Outline each Plasmodium falciparum-infected red blood cell.
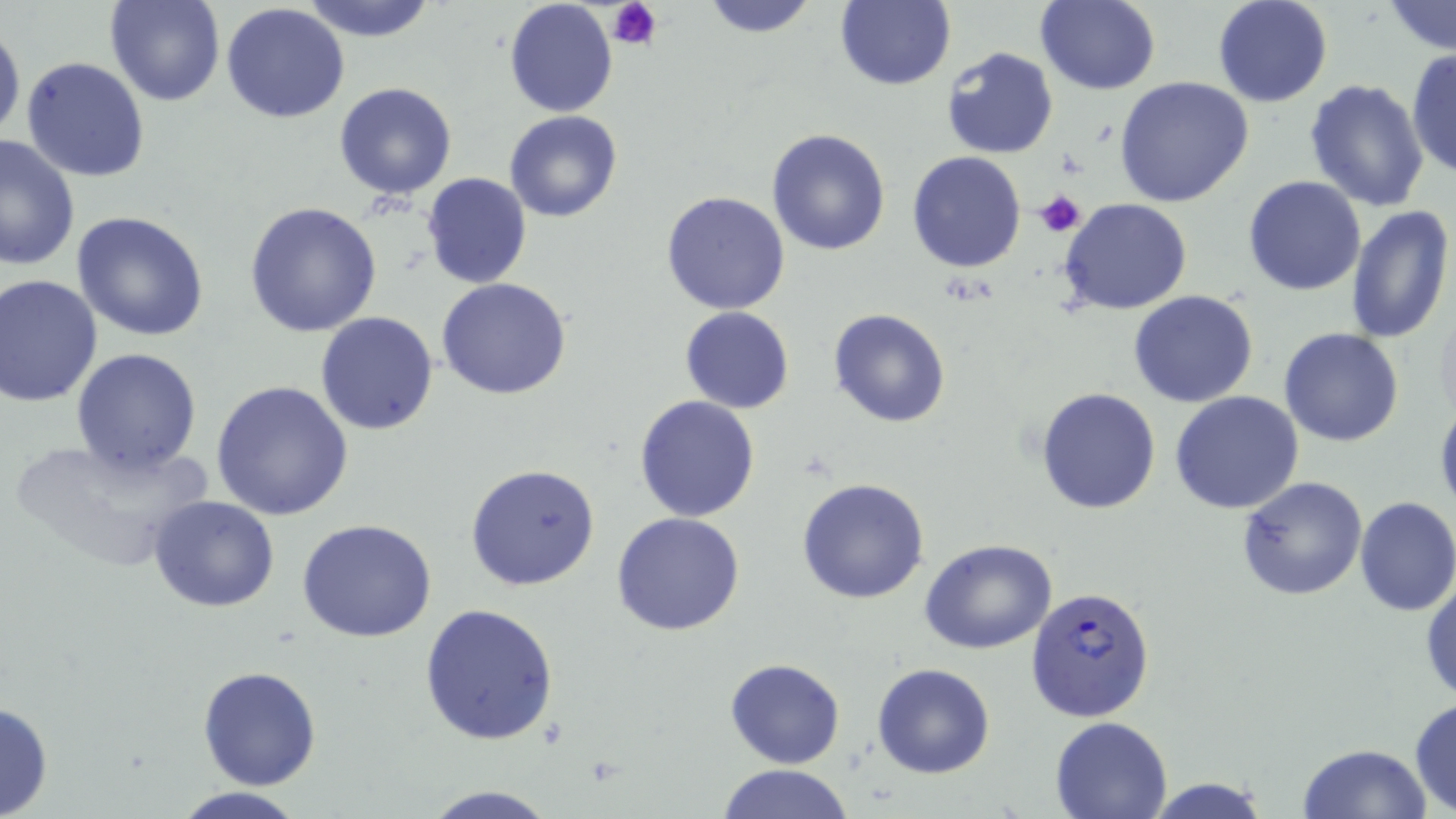
Approximate bounding boxes as (x1, y1, x2, y2) in pixels.
Plasmodium falciparum-infected red blood cells: (1025, 582, 1154, 724).

slide_level_diagnosis: Plasmodium falciparum
uninfected_red_blood_cell_locations: 'approximate bounding boxes as (x1, y1, x2, y2) in pixels: (105, 0, 226, 107), (299, 0, 438, 42), (502, 0, 619, 118), (697, 0, 825, 37), (832, 0, 956, 90), (1211, 0, 1333, 108), (1036, 1, 1162, 96), (1384, 2, 1455, 54), (221, 3, 350, 123), (0, 18, 24, 145), (943, 47, 1059, 160), (1406, 47, 1456, 181), (21, 55, 151, 184), (1113, 76, 1253, 208), (1305, 78, 1432, 213), (334, 83, 458, 200), (504, 110, 625, 223), (450, 124, 577, 251), (766, 128, 892, 256), (0, 132, 79, 271), (907, 151, 1029, 273), (421, 173, 532, 291), (1243, 176, 1366, 295), (661, 190, 791, 315), (1059, 199, 1192, 316), (244, 202, 382, 336), (1344, 203, 1454, 345), (70, 210, 210, 342), (0, 275, 102, 407), (436, 278, 572, 401), (1128, 290, 1259, 408), (680, 307, 794, 413), (828, 309, 952, 428), (315, 312, 439, 435), (1279, 328, 1404, 446), (71, 348, 202, 477), (210, 381, 354, 522), (1036, 388, 1161, 515), (1170, 391, 1305, 514), (634, 394, 761, 522), (1435, 400, 1456, 522), (10, 437, 210, 572), (466, 463, 600, 591), (1236, 477, 1369, 601), (796, 478, 930, 604), (148, 495, 279, 612), (1354, 497, 1456, 617), (612, 512, 746, 636), (298, 519, 439, 643), (919, 539, 1060, 655), (1421, 570, 1456, 704), (419, 602, 559, 745), (725, 658, 846, 768), (872, 663, 995, 779), (198, 665, 322, 790), (1408, 698, 1456, 816), (0, 700, 53, 819), (1050, 716, 1174, 818), (1299, 744, 1431, 819), (714, 764, 856, 819), (1142, 777, 1275, 818), (419, 784, 561, 819), (168, 787, 311, 819)'
field_of_view: one of a larger specimen
magnification: 1000x
modality: light microscopy
preparation: thin blood smear
stain: May-Grünwald-Giemsa
platelet_locations: 'approximate bounding boxes as (x1, y1, x2, y2) in pixels: (608, 0, 663, 49), (1034, 189, 1085, 236)'
image_size: 1456×819 pixels